Describe the morphology of the erythrocytes.
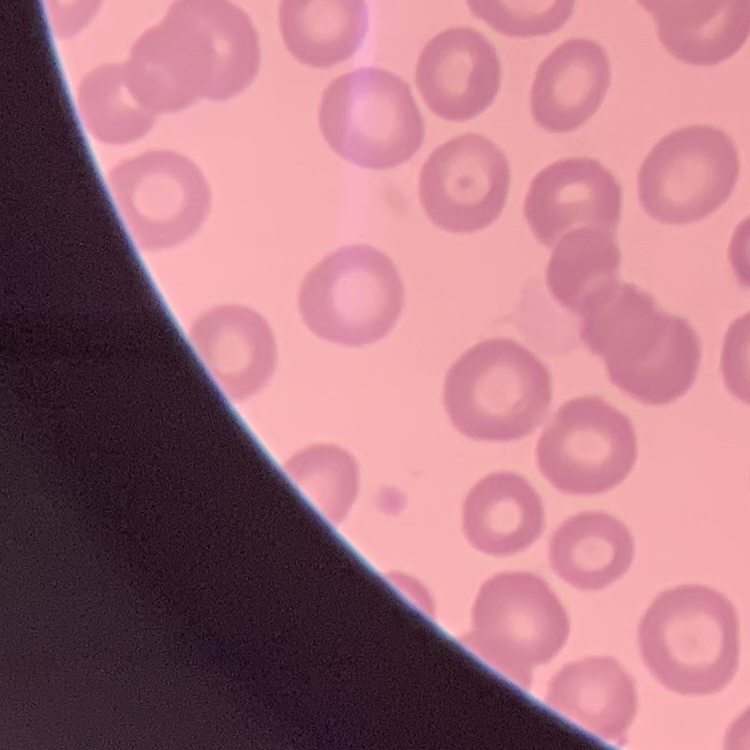

They show no rouleaux formation.

image type = one tile cut from a larger photomicrograph
preparation = thin blood smear
stain = Field's or Giemsa